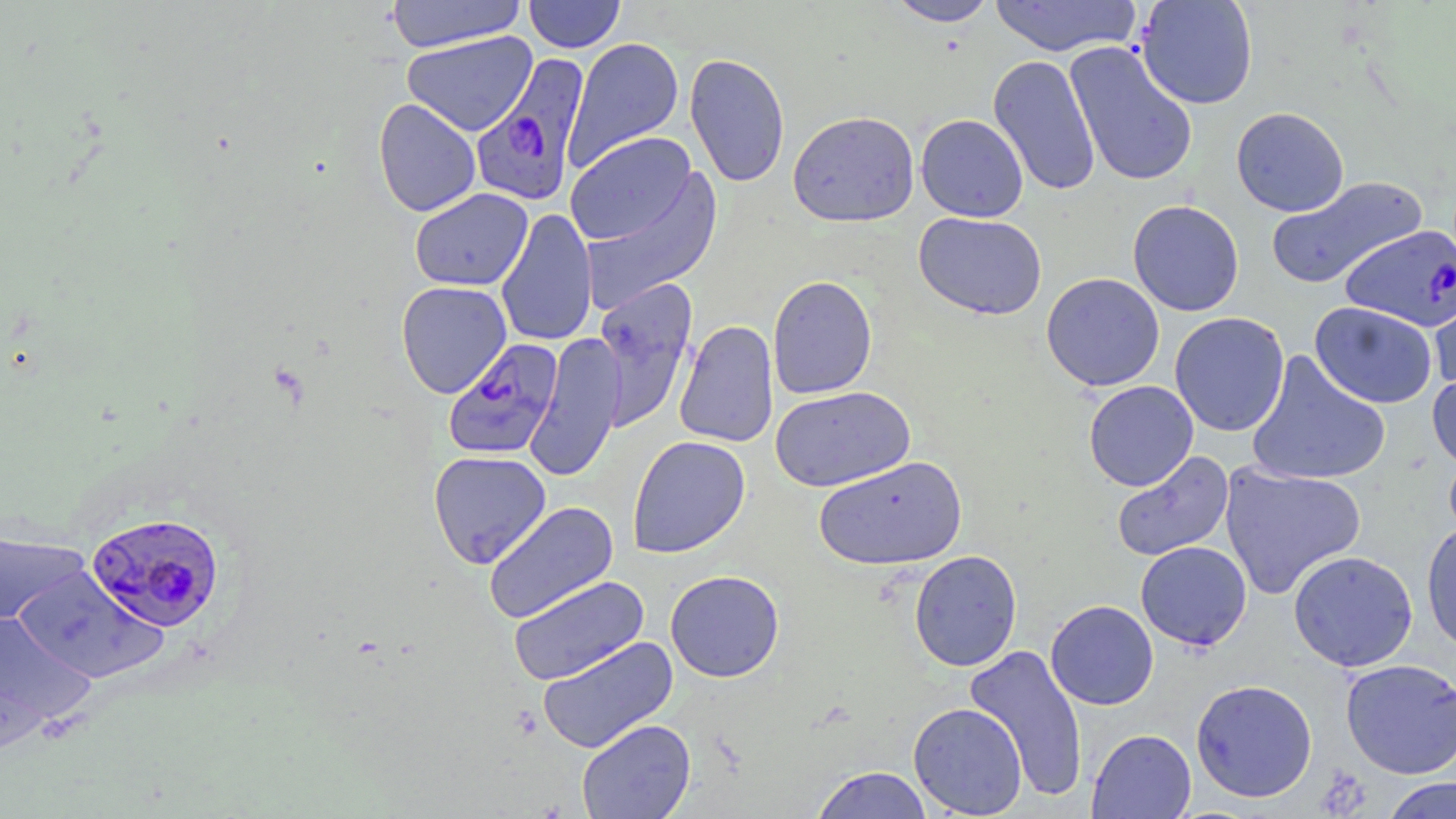 Approximate bounding boxes as (x1, y1, x2, y2) in pixels. Uninfected red blood cell locations: (386, 0, 527, 53), (524, 0, 626, 53), (887, 0, 999, 27), (989, 0, 1141, 57), (1136, 0, 1258, 110), (401, 31, 538, 137), (564, 37, 684, 172), (1064, 40, 1198, 187), (684, 52, 790, 188), (989, 54, 1101, 196), (373, 98, 481, 217), (1231, 107, 1349, 216), (787, 110, 919, 227), (915, 114, 1028, 222), (565, 133, 697, 248), (578, 168, 723, 312), (1266, 177, 1427, 289), (410, 188, 533, 291), (1127, 199, 1244, 316), (496, 208, 598, 348), (913, 212, 1047, 320), (1041, 272, 1165, 392), (1428, 272, 1456, 394), (767, 275, 878, 399), (591, 277, 698, 429), (395, 281, 512, 398), (1309, 301, 1438, 409), (1169, 312, 1289, 436), (674, 320, 779, 448), (524, 334, 627, 481), (1245, 351, 1391, 487), (1428, 367, 1456, 474), (1084, 381, 1198, 490), (770, 386, 915, 492), (627, 435, 750, 558), (428, 450, 552, 568), (1111, 450, 1234, 562), (813, 455, 967, 570), (1219, 461, 1366, 600), (483, 501, 619, 624), (1421, 521, 1456, 655), (0, 529, 90, 627), (1135, 541, 1252, 651), (908, 550, 1022, 672), (1288, 550, 1418, 671), (14, 566, 168, 682), (665, 570, 784, 682), (508, 574, 650, 685), (1045, 600, 1159, 710), (0, 612, 96, 731), (537, 635, 679, 754), (963, 643, 1089, 803), (1340, 659, 1456, 779), (1190, 679, 1317, 802), (908, 702, 1028, 818), (576, 718, 696, 819), (1086, 728, 1196, 819), (810, 766, 934, 818), (1382, 777, 1455, 819). Plasmodium falciparum-infected red blood cell locations: (473, 52, 589, 206), (1341, 224, 1456, 331), (443, 338, 565, 460), (86, 511, 225, 633). Slide-level diagnosis: Plasmodium falciparum. Thin blood film. One field of a larger specimen. Captured at 1000x magnification. Image is 1456×819 pixels. May-Grünwald-Giemsa stain. Optical microscopy.